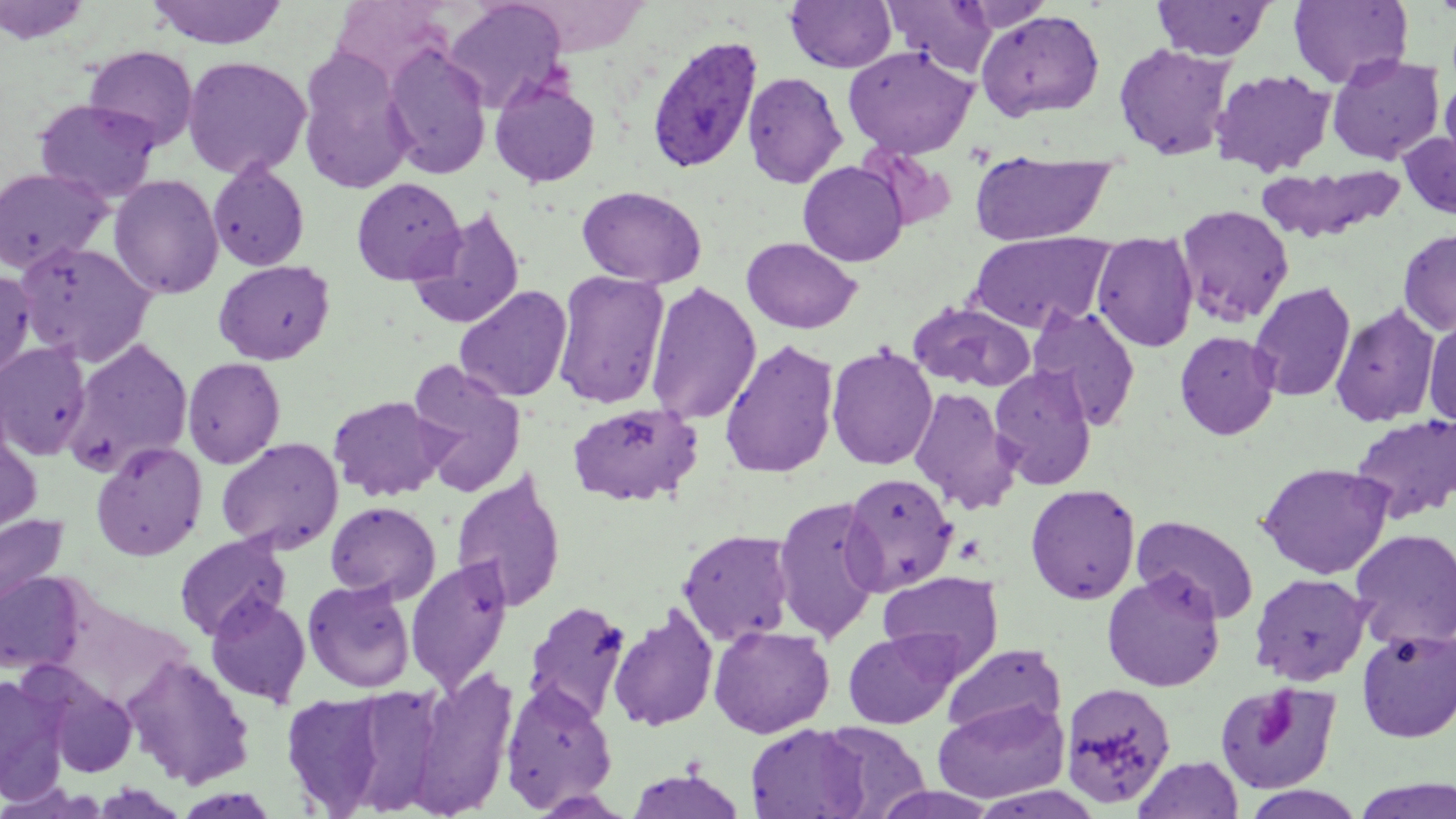

slide-level diagnosis = Plasmodium ovale
field of view = one of a larger specimen
preparation = thin blood smear
stain = May-Grünwald-Giemsa
magnification = 1000x
platelet locations = approximate bounding boxes as (x1,y1)-(x2,y2) corner pairs in pixels: (956,535)-(985,563), (1253,688)-(1299,750)
uninfected red blood cell locations = approximate bounding boxes as (x1,y1)-(x2,y2) corner pairs in pixels: (146,0)-(289,49), (443,0)-(569,113), (785,0)-(897,74), (885,0)-(999,77), (1152,0)-(1275,60), (1288,0)-(1413,89), (0,1)-(93,46), (976,10)-(1104,121), (382,42)-(492,179), (1113,42)-(1235,161), (83,45)-(199,152), (843,45)-(978,159), (296,47)-(415,193), (1326,54)-(1445,165), (182,56)-(311,180), (1210,68)-(1336,177), (742,71)-(848,188), (1440,76)-(1456,176), (489,78)-(601,187), (33,98)-(161,203), (1399,130)-(1456,221), (970,154)-(1114,245), (207,160)-(310,271), (798,161)-(908,267), (1256,163)-(1405,243), (0,167)-(113,273), (109,174)-(225,299), (350,177)-(465,285), (576,185)-(706,288), (1175,204)-(1295,327), (407,207)-(526,329), (1398,228)-(1456,336), (969,232)-(1114,333), (1092,233)-(1199,351), (741,237)-(862,334), (14,240)-(157,366), (213,260)-(335,365), (0,269)-(36,381), (553,270)-(670,410), (645,281)-(761,424), (1249,281)-(1356,402), (454,285)-(573,402), (907,301)-(1036,392), (1330,303)-(1441,426), (1027,305)-(1142,429), (1424,315)-(1456,429), (1175,330)-(1281,440), (65,338)-(194,473), (719,338)-(839,478), (0,342)-(93,460), (826,343)-(938,470), (182,357)-(286,469), (406,360)-(528,496), (989,366)-(1098,490), (908,385)-(1020,514), (327,395)-(449,501), (566,402)-(703,507), (1350,414)-(1456,523), (0,424)-(43,538), (216,437)-(344,554), (91,441)-(208,561), (1257,462)-(1393,579), (451,467)-(567,612), (842,472)-(958,593), (1026,484)-(1141,604), (772,496)-(884,643), (325,501)-(441,603), (0,513)-(72,618), (1132,515)-(1260,624), (1350,528)-(1456,650), (677,529)-(796,646), (175,533)-(290,641), (405,557)-(514,694), (1102,570)-(1225,692), (0,571)-(86,674), (878,571)-(1003,676), (1249,572)-(1372,685), (303,578)-(415,692), (205,593)-(312,707), (523,600)-(632,724), (608,605)-(719,732), (708,624)-(834,738), (1357,628)-(1455,742), (843,629)-(960,729), (943,642)-(1066,741), (120,652)-(256,788), (406,665)-(519,818), (0,672)-(68,802), (44,679)-(138,778), (1215,679)-(1342,794), (499,680)-(618,813), (1059,681)-(1176,808), (280,686)-(517,813), (281,691)-(390,815), (934,697)-(1070,803), (817,721)-(930,817), (746,724)-(869,818), (1133,756)-(1244,819), (625,769)-(747,818), (1351,778)-(1456,819), (1239,785)-(1370,819)
image size = 1456×819 pixels
Plasmodium ovale-infected red blood cell locations = approximate bounding boxes as (x1,y1)-(x2,y2) corner pairs in pixels: (645,34)-(764,175)
modality = light microscopy